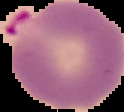
image size = 124×112 pixels
preparation = thin blood film
image type = cell region segmented out of the field of view; surrounding area masked to black
malaria status = parasitized